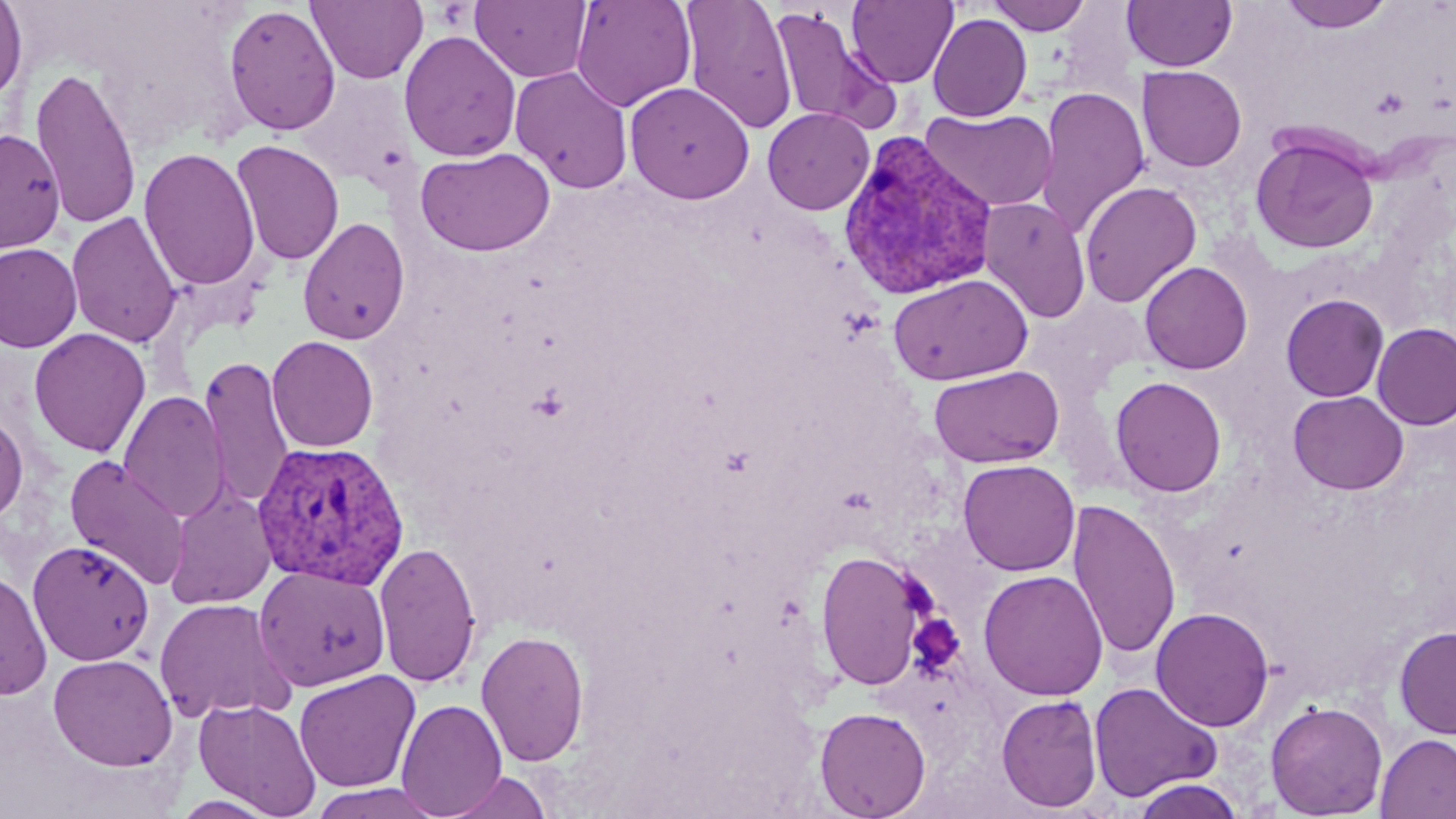 Approximate bounding boxes as (x1,y1)-(x2,y2) corner pairs in pixels. Platelet locations: (1369,87)-(1411,120), (908,614)-(964,675). Uninfected red blood cell locations: (306,0)-(428,84), (571,0)-(696,112), (680,0)-(797,133), (847,0)-(958,88), (984,0)-(1093,35), (1122,0)-(1237,71), (1280,0)-(1394,32), (0,1)-(27,104), (471,1)-(592,83), (223,4)-(341,136), (769,6)-(893,132), (927,14)-(1032,122), (398,30)-(522,162), (509,64)-(633,194), (30,65)-(142,231), (1138,65)-(1247,171), (293,73)-(416,189), (624,81)-(754,203), (1035,86)-(1150,238), (922,107)-(1057,212), (762,108)-(874,215), (0,128)-(66,254), (1251,134)-(1379,254), (231,139)-(344,265), (139,147)-(260,292), (415,147)-(556,256), (1079,181)-(1202,308), (978,196)-(1091,323), (66,211)-(182,348), (297,217)-(411,345), (0,243)-(82,353), (1139,261)-(1253,374), (888,273)-(1033,386), (1281,294)-(1389,402), (1372,322)-(1456,429), (29,328)-(151,457), (266,335)-(379,452), (199,355)-(295,510), (929,365)-(1064,469), (1110,375)-(1227,497), (1288,390)-(1409,494), (118,391)-(230,524), (0,409)-(28,525), (64,455)-(191,590), (956,459)-(1079,576), (165,485)-(277,609), (1068,499)-(1181,660), (27,539)-(155,666), (374,541)-(482,687), (815,549)-(930,691), (254,566)-(391,691), (0,569)-(52,700), (978,569)-(1109,701), (153,597)-(295,722), (1151,607)-(1274,731), (1393,625)-(1456,739), (476,630)-(589,766), (48,653)-(177,771), (294,670)-(420,792), (1088,681)-(1222,803), (996,693)-(1103,813), (195,697)-(322,816), (396,698)-(506,817), (1266,700)-(1388,818), (814,706)-(931,819), (1375,733)-(1456,819), (442,770)-(552,818), (1129,777)-(1246,818), (309,783)-(447,819). Plasmodium vivax-infected red blood cell locations: (835,130)-(999,302), (252,439)-(409,590). Slide-level diagnosis: Plasmodium vivax. Light microscopy. Thin blood smear. One field of a larger specimen. May-Grünwald-Giemsa stain. Captured at 1000x magnification. Image is 1456×819 pixels.